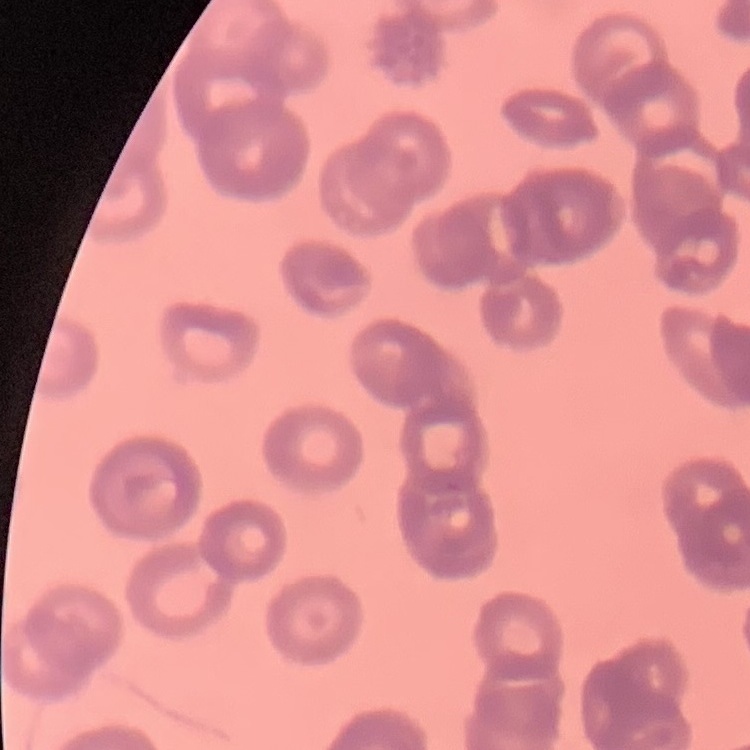
Summary:
  - Red blood cell morphology: rouleaux formation
  - Image type: square crop of a larger photomicrograph
  - Preparation: thin blood smear
  - Stain: Field's or Giemsa